Identify the parasite.
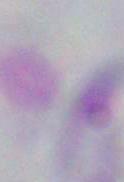
This is Toxoplasma gondii.

Summary:
  - Magnification: 1000x
  - Modality: photomicrograph